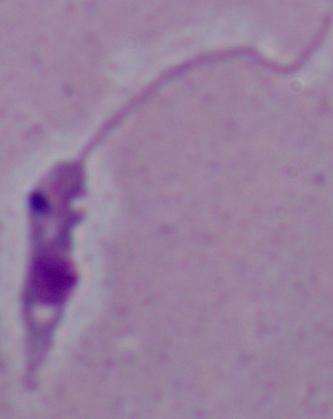

Summary:
  - Modality: micrograph
  - Identification: Leishmania
  - Magnification: 1000x